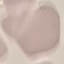
{
  "malaria_status": "uninfected",
  "stain": "Giemsa",
  "preparation": "thin blood film",
  "capture": "smartphone through the microscope eyepiece",
  "image_type": "automatically extracted cell patch, resized to 64 × 64 pixels"
}